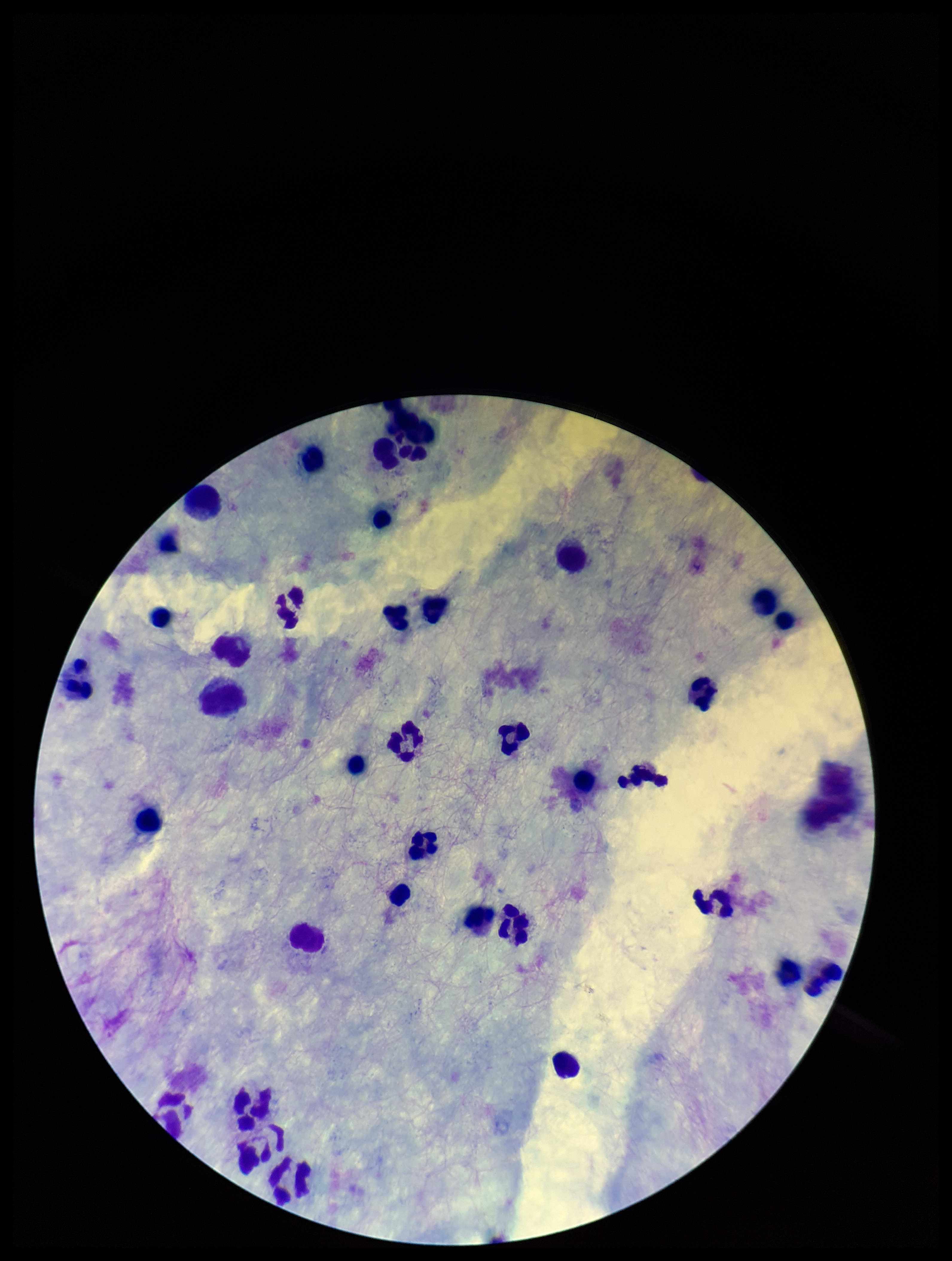

patient malaria status = negative
leukocyte count = 31
Plasmodium parasites = none seen
preparation = thick blood smear
capture = smartphone photograph through the microscope eyepiece
field of view = single
image size = 952×1261 pixels
parasite count = 0
stain = Giemsa